Assess this cell for malaria.
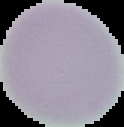

It is uninfected.

Summary:
  - Image type: segmented cell region with the area outside set to black
  - Preparation: thin blood smear
  - Image size: 124×127 pixels